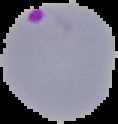

Summary:
  - Image size: 118×124 pixels
  - Image type: cell region segmented out of the field of view; surrounding area masked to black
  - Result: Plasmodium parasites identified
  - Preparation: thin blood film